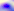 Micrograph. 400x magnification. Toxoplasma gondii is shown.